Assess this cell for malaria.
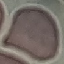
It is uninfected.

capture: smartphone through the microscope eyepiece
preparation: thin smear
image_type: automatically extracted cell patch, resized to 64 × 64 pixels
stain: Giemsa